Comment on the morphology of the erythrocytes.
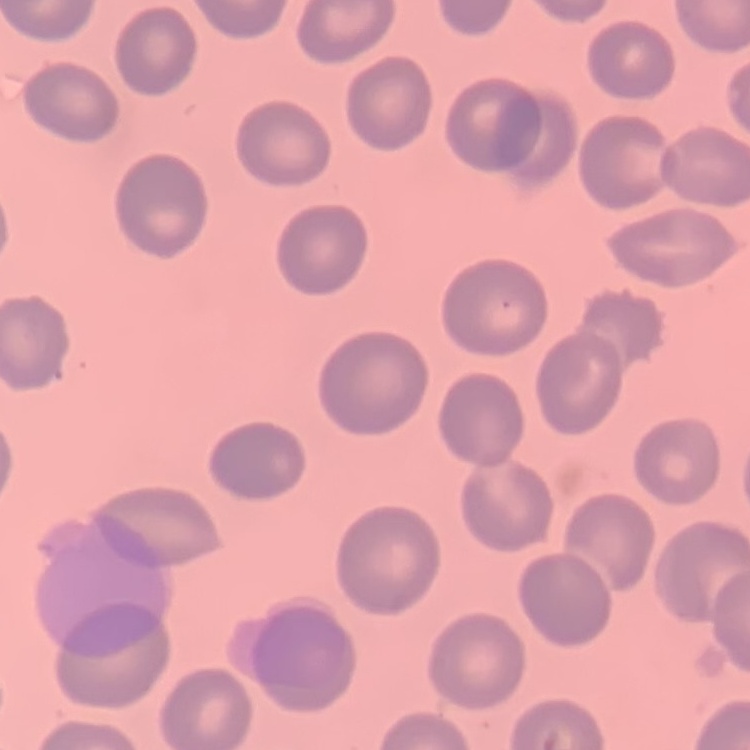
No rouleaux formation.

Thin blood smear. Square crop of a larger photomicrograph. Stained with either Field's or Giemsa.